Outline platelets.
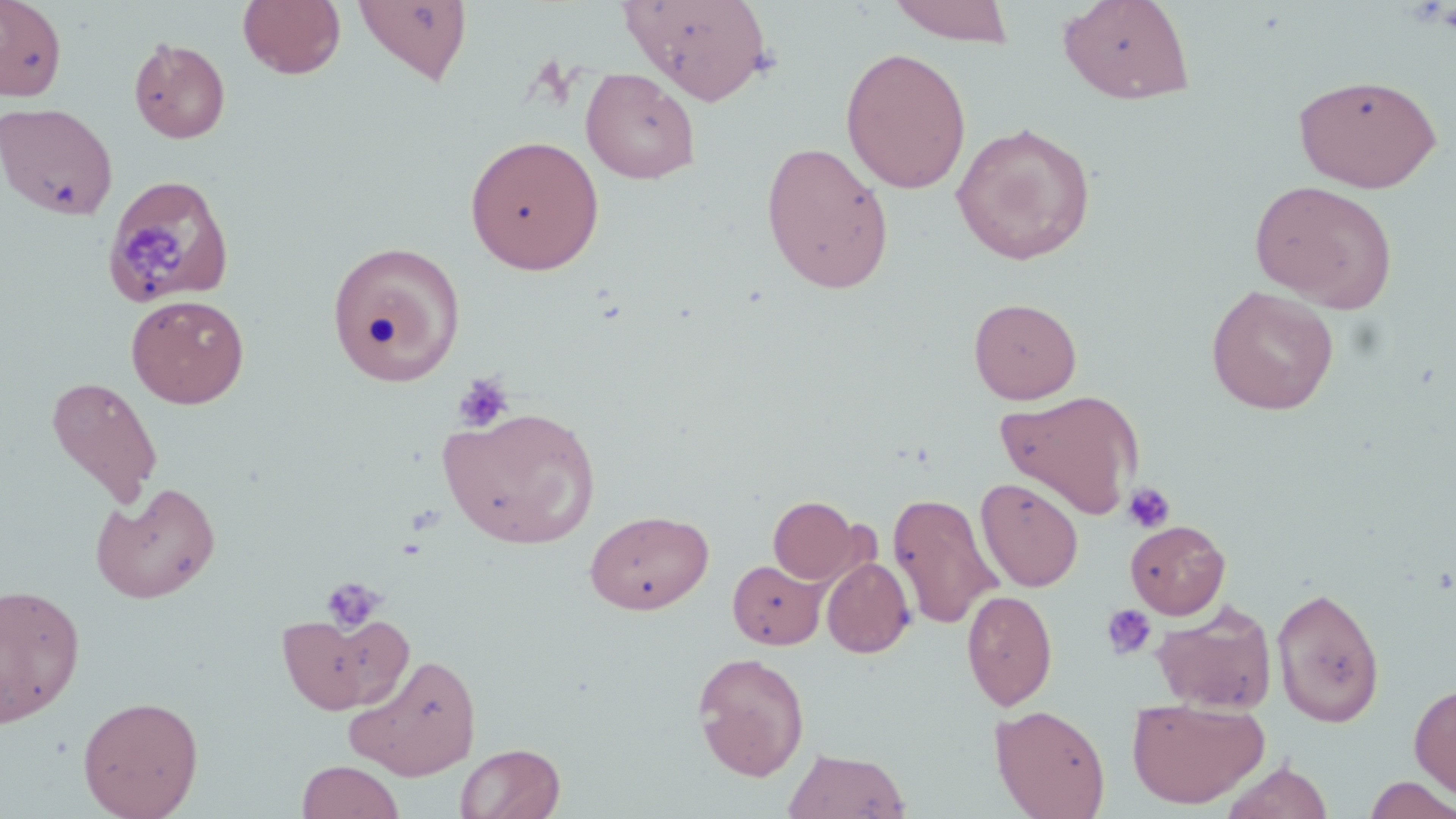

Approximate bounding boxes as (x1, y1, x2, y2) in pixels.
Platelets: (122, 222, 188, 296), (452, 373, 515, 433), (1123, 482, 1175, 533), (321, 575, 386, 633), (1100, 603, 1158, 661).

slide-level diagnosis = no evidence of blood parasites
magnification = 1000x
stain = May-Grünwald-Giemsa
uninfected red blood cell locations = approximate bounding boxes as (x1, y1, x2, y2) in pixels: (0, 0, 67, 101), (237, 0, 346, 80), (353, 0, 472, 87), (622, 0, 774, 106), (887, 0, 1017, 46), (1058, 0, 1195, 104), (128, 36, 231, 144), (840, 47, 972, 194), (580, 67, 701, 184), (1292, 74, 1443, 192), (0, 102, 118, 219), (951, 122, 1097, 265), (465, 133, 604, 275), (760, 140, 895, 294), (103, 175, 237, 309), (1249, 179, 1399, 311), (326, 239, 467, 385), (1206, 286, 1340, 415), (126, 294, 249, 409), (969, 297, 1081, 404), (44, 376, 163, 510), (995, 388, 1144, 520), (438, 406, 600, 549), (976, 476, 1083, 592), (91, 482, 221, 603), (888, 492, 1001, 630), (768, 496, 863, 584), (584, 509, 714, 614), (1126, 520, 1231, 618), (822, 557, 916, 658), (728, 559, 827, 649), (0, 582, 85, 726), (1271, 586, 1385, 728), (962, 589, 1057, 710), (1151, 600, 1278, 713), (277, 614, 408, 715), (345, 652, 482, 780), (692, 652, 810, 781), (1409, 682, 1456, 804), (77, 695, 204, 818), (1126, 697, 1270, 809), (990, 704, 1111, 819), (455, 742, 565, 819), (783, 748, 911, 819), (296, 760, 405, 819), (1220, 760, 1334, 819), (1362, 774, 1456, 818)
image size = 1456×819 pixels
field of view = single
preparation = thin blood smear
modality = optical microscopy